Point out leukocytes.
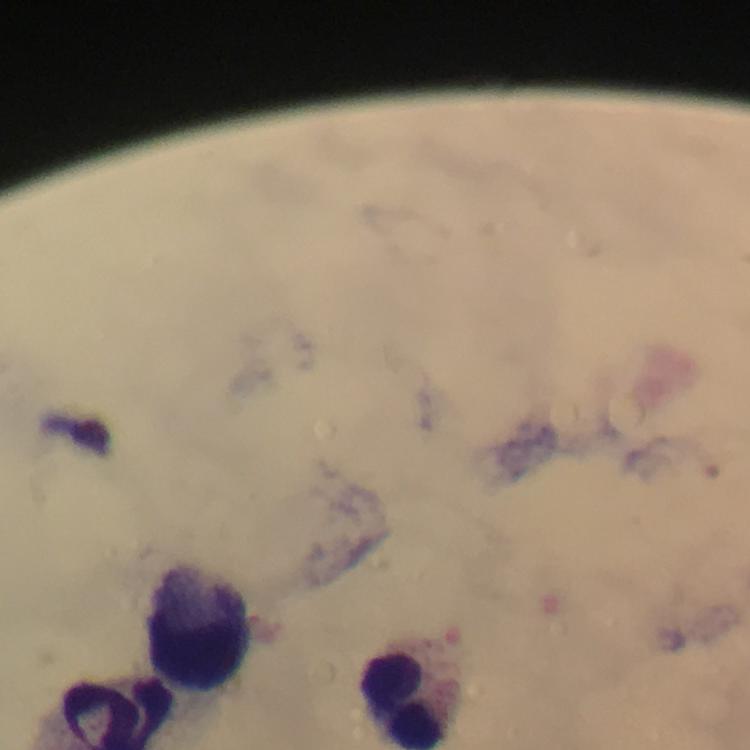
Approximate centers as [x, y] in pixels.
Leukocytes: [199, 626], [405, 700].

Plasmodium parasites = none detected
immersion oil = applied
stain = Giemsa
capture = smartphone mounted on the microscope
magnification = 100x
preparation = thick blood smear
cropped from = one field of view
image size = 750×750 pixels
context = from a diagnostic examination for malaria